Report the malaria status of this cell.
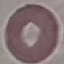

It is uninfected.

Photographed with a smartphone camera at the microscope eyepiece. Thin blood smear. Giemsa stain. Cell patch, automatically extracted from a larger field of view and resized to 64 × 64 pixels.